Give the position of every Plasmodium parasite.
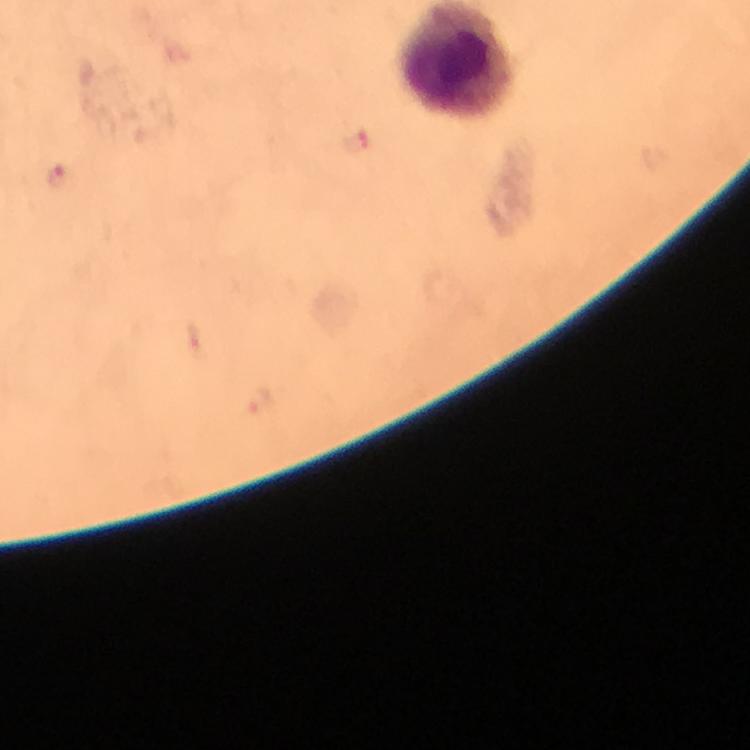
Approximate object centers, in pixels from the top-left corner.
Plasmodium parasites: (x=356, y=145), (x=56, y=177).

capture = smartphone photograph through a microscope
preparation = thick blood smear
stain = Giemsa
magnification = 100x
image size = 750×750 pixels
cropped from = one field of view
immersion oil = applied
context = from a malaria diagnostic workup